Give the position of every Plasmodium parasite visible.
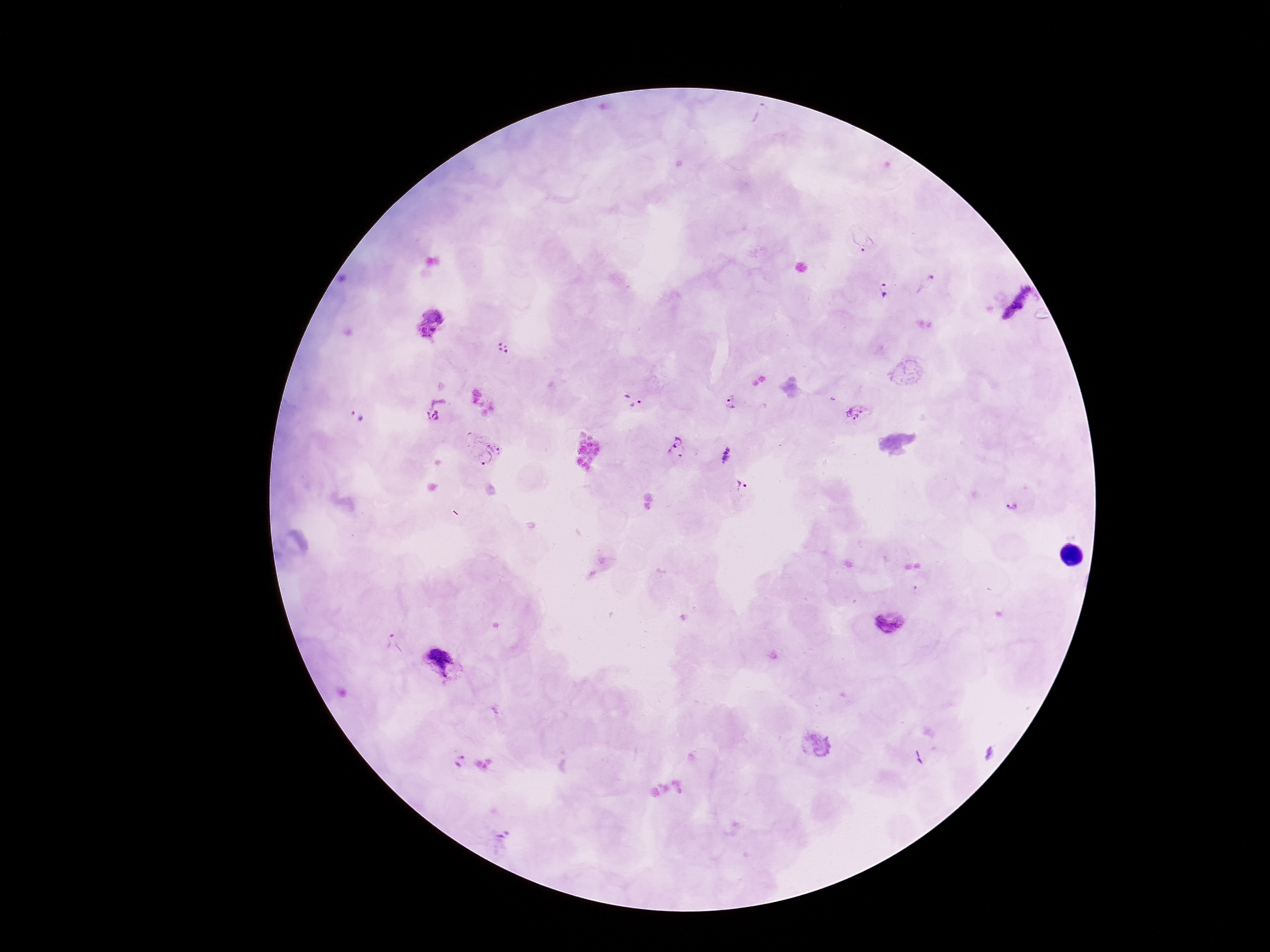

Approximate centers as [x, y] in pixels.
Plasmodium parasites: [863, 239], [925, 284], [883, 292], [1017, 302], [430, 323], [504, 348], [632, 400], [732, 402], [436, 410], [855, 414], [357, 417], [677, 448], [482, 449], [726, 456], [741, 484], [1013, 507], [890, 626], [389, 643], [439, 659], [457, 758].

Summary:
  - Capture: smartphone camera through the microscope eyepiece
  - Preparation: thick blood film
  - Stain: Giemsa
  - Magnification: 100x
  - Field of view: one from this slide
  - Image size: 1270×952 pixels
  - Patient malaria status: positive